Locate every Plasmodium malariae-infected red blood cell.
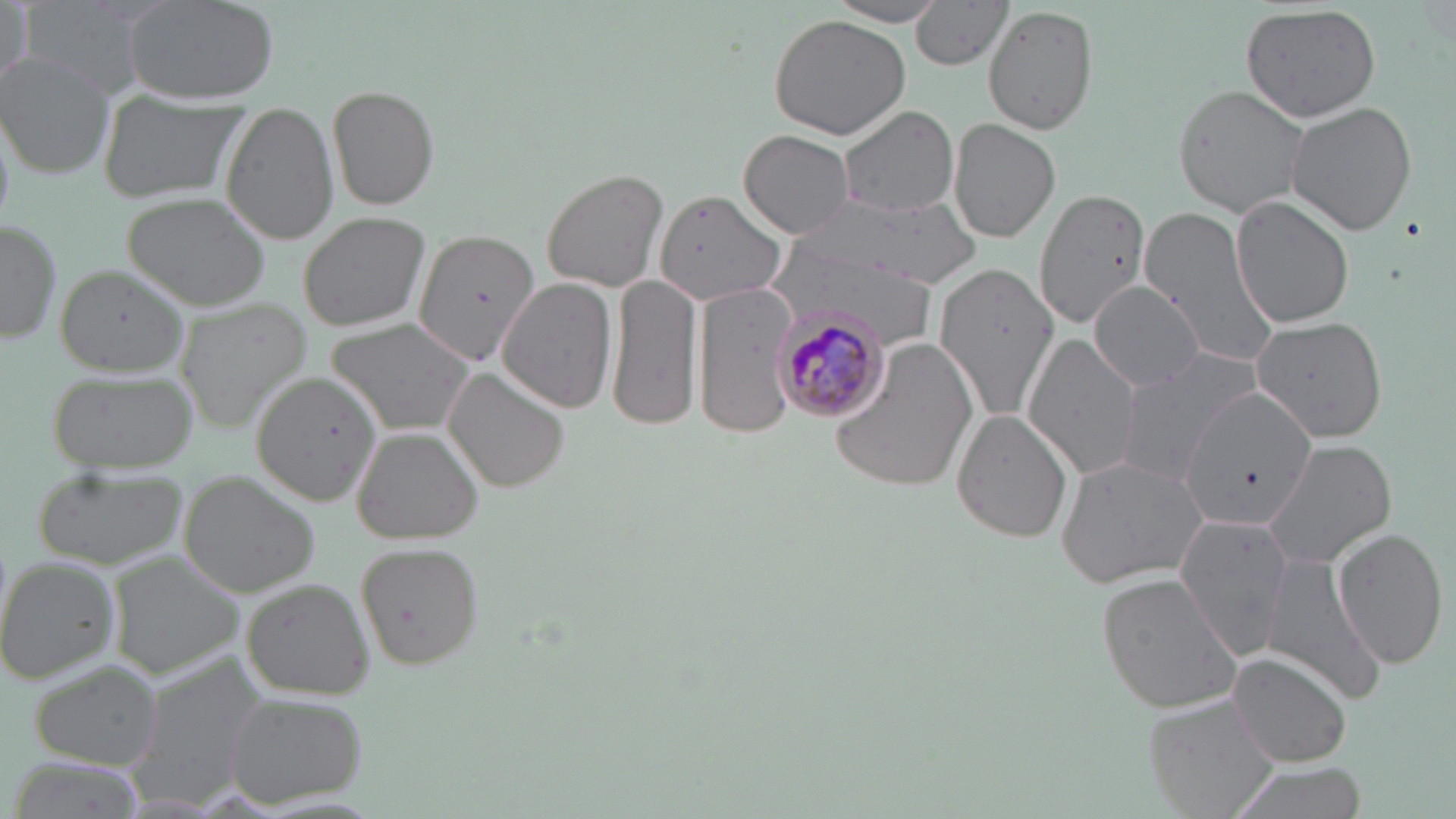
Approximate bounding boxes as (x1,y1)-(x2,y2) corner pairs in pixels.
Plasmodium malariae-infected red blood cells: (770,306)-(894,423).

slide_level_diagnosis: Plasmodium malariae
image_size: 1456×819 pixels
stain: May-Grünwald-Giemsa
modality: light microscopy
magnification: 1000x
preparation: thin blood film
field_of_view: one of a larger specimen
uninfected_red_blood_cell_locations: 'approximate bounding boxes as (x1,y1)-(x2,y2) corner pairs in pixels: (1,0)-(33,95), (18,0)-(161,101), (121,0)-(278,107), (910,0)-(1015,71), (829,1)-(947,26), (1241,4)-(1382,124), (983,5)-(1099,136), (767,15)-(912,139), (0,56)-(115,179), (327,85)-(440,211), (1173,85)-(1309,218), (99,92)-(244,202), (1285,100)-(1418,236), (224,102)-(338,245), (838,107)-(959,220), (950,118)-(1061,242), (739,129)-(852,237), (540,167)-(669,292), (1033,186)-(1150,332), (658,190)-(787,305), (809,192)-(972,291), (123,193)-(271,311), (1231,195)-(1354,330), (1141,206)-(1281,370), (296,210)-(433,333), (0,219)-(61,345), (414,229)-(548,371), (767,233)-(946,353), (936,260)-(1059,420), (55,264)-(193,374), (606,270)-(705,435), (498,279)-(618,413), (695,282)-(800,439), (1090,284)-(1208,390), (177,299)-(312,429), (326,316)-(478,437), (1250,317)-(1388,442), (1024,335)-(1142,481), (827,337)-(979,492), (1113,350)-(1262,488), (442,368)-(569,493), (48,369)-(197,471), (253,371)-(380,508), (950,409)-(1075,543), (354,428)-(483,546), (1263,438)-(1396,571), (1055,453)-(1213,588), (31,466)-(187,569), (179,472)-(321,597), (1174,514)-(1292,659), (1334,529)-(1449,669), (353,540)-(484,670), (1259,549)-(1386,702), (110,554)-(245,676), (0,556)-(120,684), (1097,572)-(1245,716), (241,578)-(375,698), (1229,651)-(1353,768), (130,652)-(272,801), (28,659)-(166,768), (223,692)-(367,808), (1147,697)-(1283,819), (1226,760)-(1370,819)'